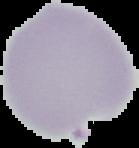 Image is 139×148 pixels. From a thin blood smear. Segmented cell region on a black background. Result: malaria parasites identified.